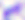

Summary:
  - Modality: micrograph
  - Identification: Toxoplasma gondii
  - Magnification: 400x